Describe the morphology of the red blood cells.
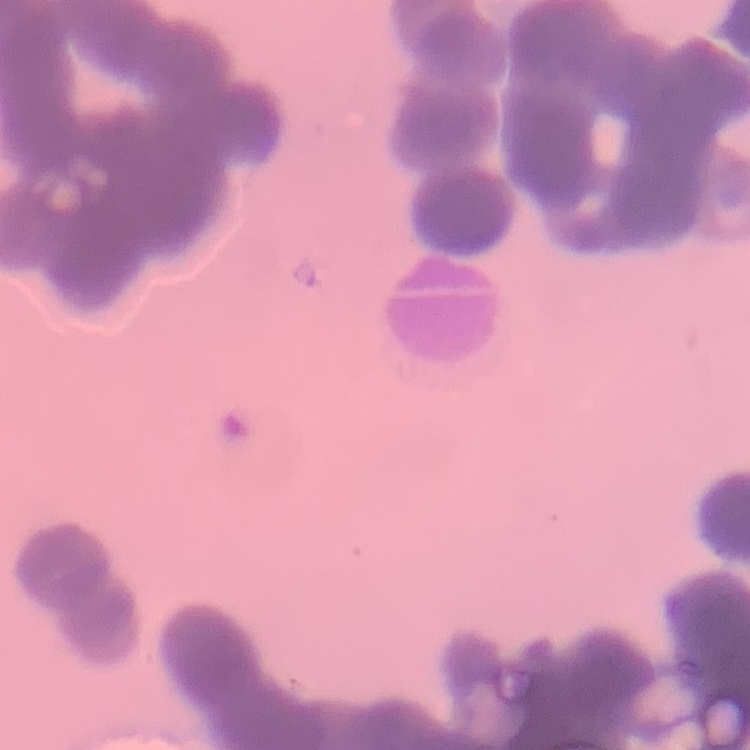
Rouleaux formation.

stain = Field's or Giemsa
image type = square crop of a larger photomicrograph
preparation = thin peripheral smear